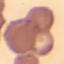 Result: no malaria parasites seen. Giemsa stain. Automatically extracted cell patch, resized to 64 × 64 pixels. Thin smear of blood. Photographed with a smartphone camera at the microscope eyepiece.